Assess this cell for malaria.
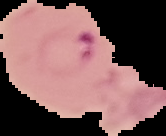
Parasitized.

The area outside the segmented cell region is set to black. Image is 166×136 pixels. From a thin blood smear.